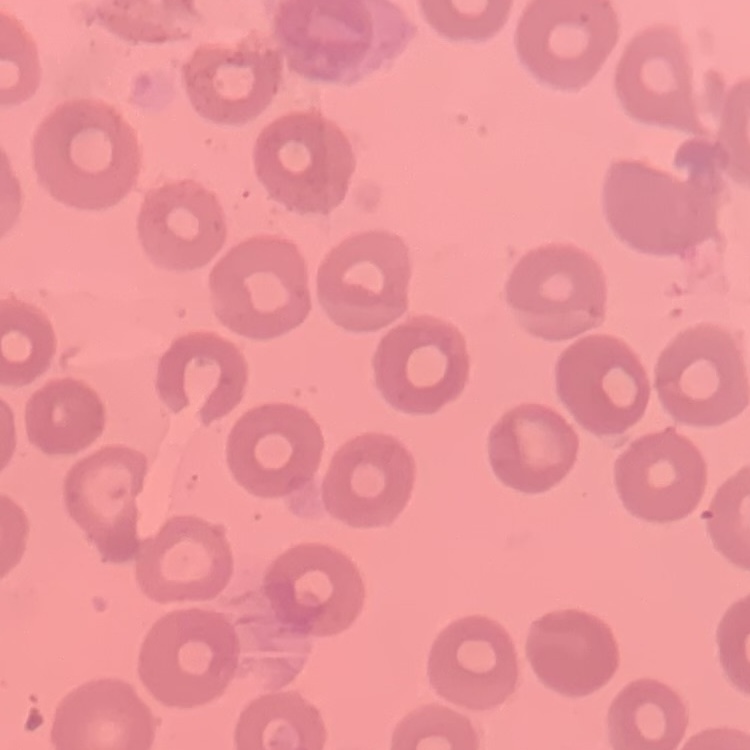
{
  "erythrocyte_morphology": "no rouleaux formation",
  "stain": "Field's or Giemsa",
  "image_type": "square crop of a larger photomicrograph",
  "preparation": "thin peripheral smear"
}